Assess this cell for malaria.
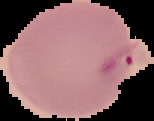

Uninfected.

Summary:
  - Image type: segmented cell region on a black background
  - Image size: 154×121 pixels
  - Preparation: thin blood film